Assess this cell for malaria.
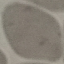

Uninfected.

Summary:
  - Image type: cell patch, automatically extracted from a larger field of view and resized to 64 × 64 pixels
  - Preparation: thin smear
  - Stain: Giemsa
  - Capture: smartphone through the microscope eyepiece